Identify the preparation type.
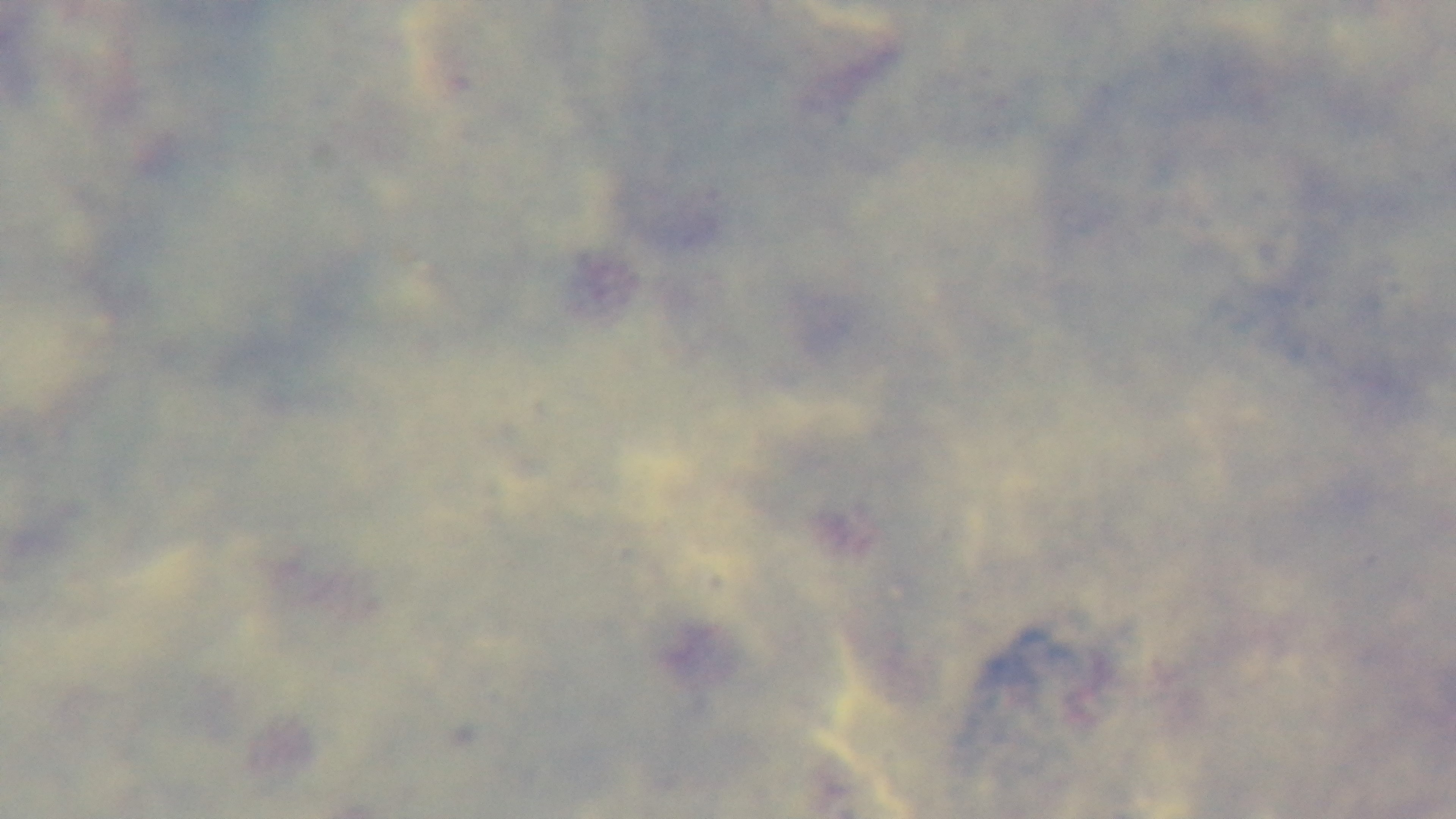

A thick smear.

stain: Giemsa
field_of_view: one from the slide
capture: mounted 4K digital camera
modality: light microscopy
objective: 100x oil immersion
malaria_status: uninfected